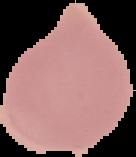 From a thin blood film. Image is 136×157 pixels. Malaria status: uninfected. Cell region segmented out of the field of view; the surrounding area is masked to black.